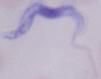

A trypanosome is shown. Micrograph. Captured at 1000x magnification.